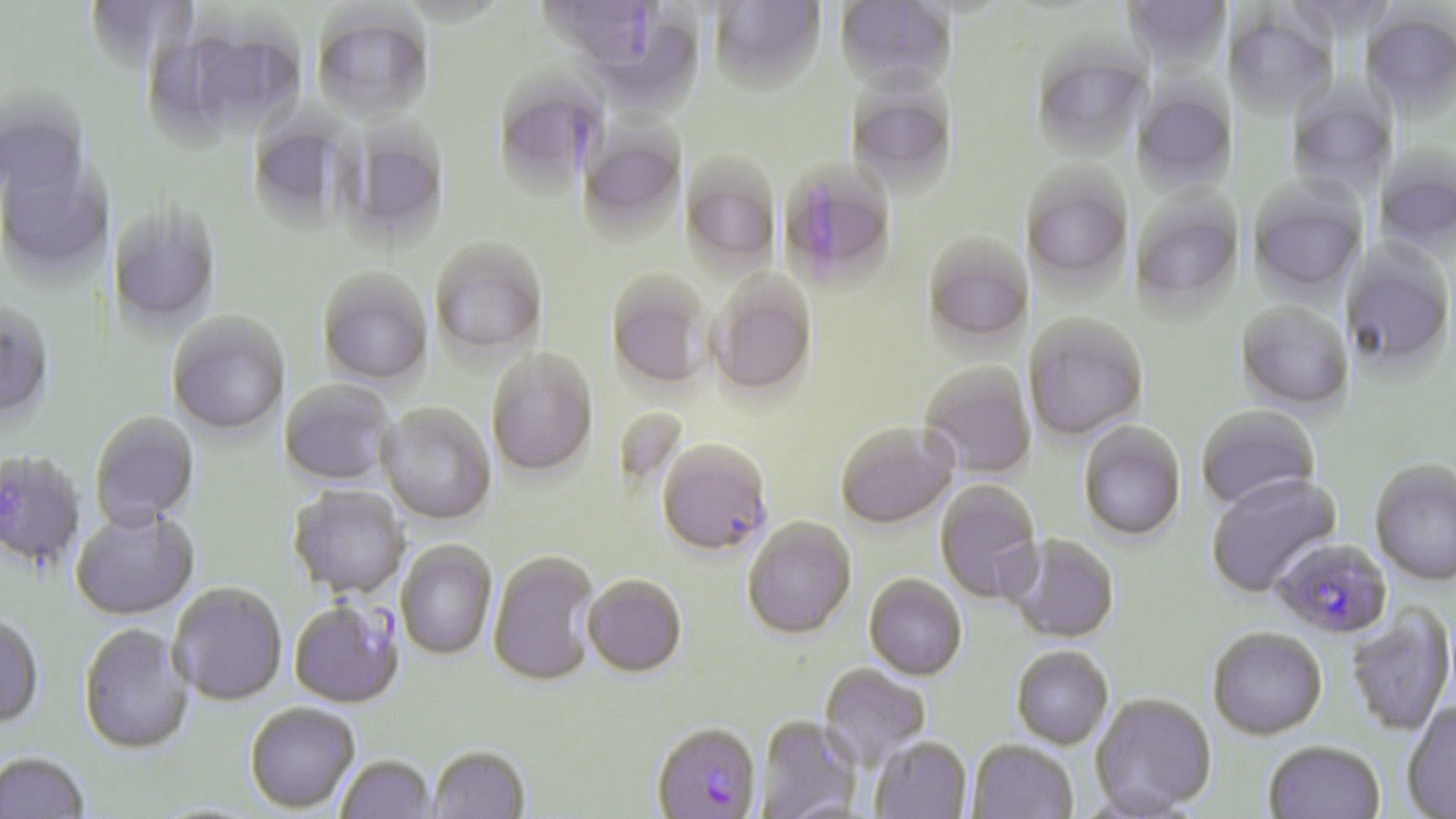
Plasmodium falciparum-infected red blood cell locations = approximate bounding boxes as (x1,y1)-(x2,y2) corner pairs in pixels: (538,1)-(667,76), (775,161)-(900,292), (657,442)-(773,558), (1271,540)-(1393,641), (288,602)-(403,710), (651,726)-(763,819)
slide-level diagnosis = Plasmodium falciparum
stain = May-Grünwald-Giemsa
field of view = one of a larger specimen
preparation = thin blood film
image size = 1456×819 pixels
magnification = 1000x
modality = light microscopy
uninfected red blood cell locations = approximate bounding boxes as (x1,y1)-(x2,y2) corner pairs in pixels: (84,0)-(199,75), (707,0)-(827,99), (833,0)-(957,101), (1118,1)-(1231,73), (580,10)-(705,117), (1361,10)-(1456,120), (1223,12)-(1338,120), (311,13)-(433,125), (151,18)-(307,143), (1031,45)-(1152,161), (492,75)-(607,196), (845,84)-(959,196), (1285,86)-(1397,199), (1130,87)-(1239,196), (245,111)-(355,230), (576,115)-(688,241), (333,118)-(451,247), (0,148)-(111,280), (1374,150)-(1456,257), (678,153)-(781,276), (1022,164)-(1134,289), (1247,180)-(1367,298), (1128,187)-(1246,318), (107,205)-(221,329), (923,234)-(1033,349), (1342,239)-(1455,374), (430,240)-(548,363), (316,270)-(433,388), (605,271)-(712,392), (708,273)-(818,400), (1235,302)-(1354,412), (0,305)-(54,425), (167,314)-(290,437), (1025,315)-(1148,443), (487,352)-(598,479), (920,363)-(1036,478), (279,380)-(394,487), (378,404)-(496,526), (1196,406)-(1321,513), (90,414)-(200,532), (835,423)-(959,531), (1078,423)-(1186,542), (0,452)-(86,572), (1369,461)-(1456,587), (1206,475)-(1342,598), (934,480)-(1044,605), (288,487)-(407,600), (71,509)-(199,621), (743,519)-(857,642), (1005,536)-(1120,644), (396,541)-(496,660), (487,553)-(601,689), (582,576)-(687,680), (863,576)-(967,682), (168,585)-(287,708), (1346,606)-(1454,737), (0,618)-(44,730), (77,626)-(194,758), (1207,630)-(1328,742), (1011,648)-(1113,751), (818,664)-(931,770), (1089,695)-(1217,818), (1402,703)-(1456,817), (244,704)-(360,815), (755,717)-(861,819), (869,739)-(972,819), (966,741)-(1078,819), (1263,743)-(1385,819), (427,749)-(530,819), (0,755)-(89,818), (336,757)-(436,819)